Describe the morphology of the red blood cells.
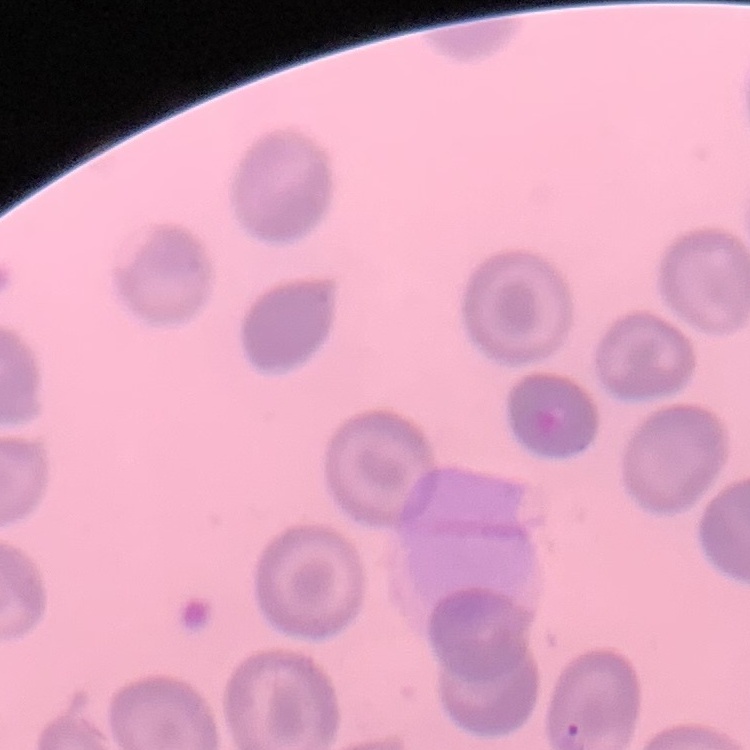

They show no rouleaux formation.

Summary:
  - Preparation: thin peripheral smear
  - Stain: Field's or Giemsa
  - Image type: one tile cut from a larger photomicrograph